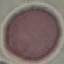
malaria status = uninfected
image type = cell patch, automatically extracted from a larger field of view and resized to 64 × 64 pixels
stain = Giemsa
preparation = thin blood smear
capture = smartphone through the microscope eyepiece